Report the malaria status of this cell.
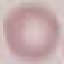
It is uninfected.

Giemsa stain. Thin smear of blood. Automatically extracted cell patch, resized to 64 × 64 pixels. Acquired by smartphone through the microscope eyepiece.